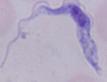

identification = trypanosome
magnification = 1000x
modality = photomicrograph